Identify the parasite.
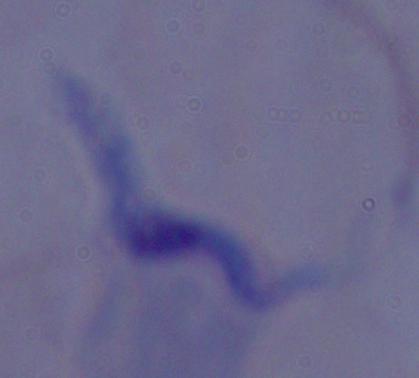

A trypanosome.

Summary:
  - Magnification: 1000x
  - Modality: micrograph